Assess this cell for malaria.
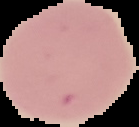
It is uninfected.

Summary:
  - Preparation: thin blood smear
  - Image size: 139×127 pixels
  - Image type: segmented cell region on a black background